Give the extent of all Plasmodium falciparum-infected red blood cells.
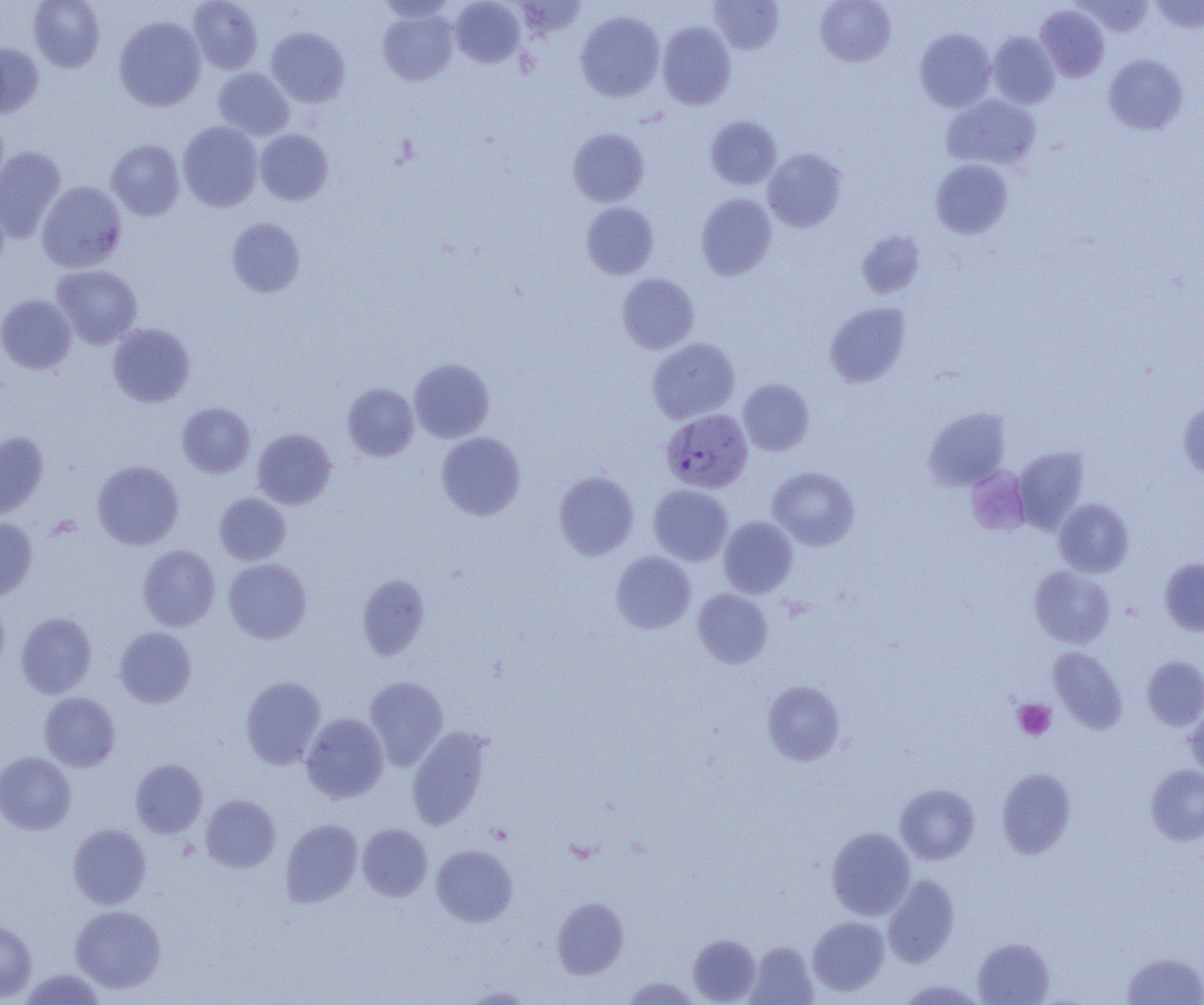

Approximate bounding boxes as (x1, y1, x2, y2) in pixels.
Plasmodium falciparum-infected red blood cells: (661, 408, 753, 493).

Platelet locations (subset): (1013, 699, 1056, 741). Uninfected red blood cell locations (subset): (29, 0, 105, 72), (188, 0, 263, 75), (450, 0, 525, 68), (815, 0, 896, 67), (1076, 0, 1155, 37), (1150, 0, 1204, 33), (711, 1, 784, 54), (1035, 5, 1109, 82), (378, 9, 458, 85), (575, 11, 665, 101), (114, 16, 206, 111), (658, 21, 736, 110), (267, 28, 350, 106), (915, 29, 996, 112), (987, 31, 1060, 108), (0, 43, 43, 118), (1104, 54, 1187, 135), (213, 67, 294, 140), (942, 94, 1041, 170), (705, 116, 782, 189), (178, 122, 263, 211), (568, 128, 649, 207), (255, 130, 333, 205), (107, 139, 185, 220), (0, 147, 66, 243), (763, 148, 847, 232), (930, 159, 1013, 238), (37, 181, 127, 272), (696, 193, 777, 280), (581, 201, 659, 279), (227, 218, 306, 297), (51, 264, 142, 348), (617, 273, 699, 354), (0, 294, 77, 374), (825, 303, 911, 387), (108, 322, 195, 407), (647, 337, 740, 424), (409, 358, 495, 443), (738, 378, 814, 456), (342, 383, 419, 461), (1177, 401, 1204, 480), (177, 402, 255, 477), (924, 408, 1010, 490), (252, 428, 336, 509), (0, 432, 48, 521), (436, 432, 526, 520), (1012, 447, 1089, 533), (92, 460, 184, 550), (768, 466, 860, 550), (554, 470, 639, 560), (555, 478, 732, 561), (648, 484, 733, 565), (214, 493, 290, 565), (1054, 499, 1134, 577), (719, 517, 798, 598), (0, 518, 37, 602), (138, 545, 220, 631), (611, 551, 696, 634), (224, 558, 311, 643), (1160, 558, 1204, 636), (1029, 566, 1115, 648), (357, 574, 429, 660), (693, 589, 773, 669), (0, 597, 10, 677), (16, 612, 97, 698), (114, 627, 197, 708), (1048, 647, 1127, 733), (1142, 655, 1204, 730), (240, 676, 326, 769), (364, 676, 448, 770), (762, 680, 845, 765), (39, 692, 120, 772), (1185, 705, 1204, 777), (301, 712, 388, 803), (407, 726, 492, 830), (0, 751, 76, 834), (130, 759, 207, 838), (1146, 765, 1204, 845), (996, 768, 1076, 859), (895, 784, 979, 865), (200, 794, 280, 872), (280, 819, 363, 907), (357, 823, 432, 901), (68, 824, 151, 909), (826, 827, 915, 920), (431, 844, 517, 927), (883, 874, 959, 968), (552, 897, 629, 979), (70, 905, 166, 993), (807, 916, 890, 995), (0, 919, 37, 1002), (688, 934, 761, 1004), (973, 937, 1055, 1005), (745, 941, 818, 1004), (1122, 951, 1204, 1005), (19, 968, 107, 1005), (620, 976, 702, 1004), (896, 979, 988, 1005), (458, 985, 539, 1004). Slide-level diagnosis: Plasmodium falciparum. Optical microscopy. One field of a larger specimen. Captured at 1000x magnification. Thin blood film. Image is 1204×1005 pixels.